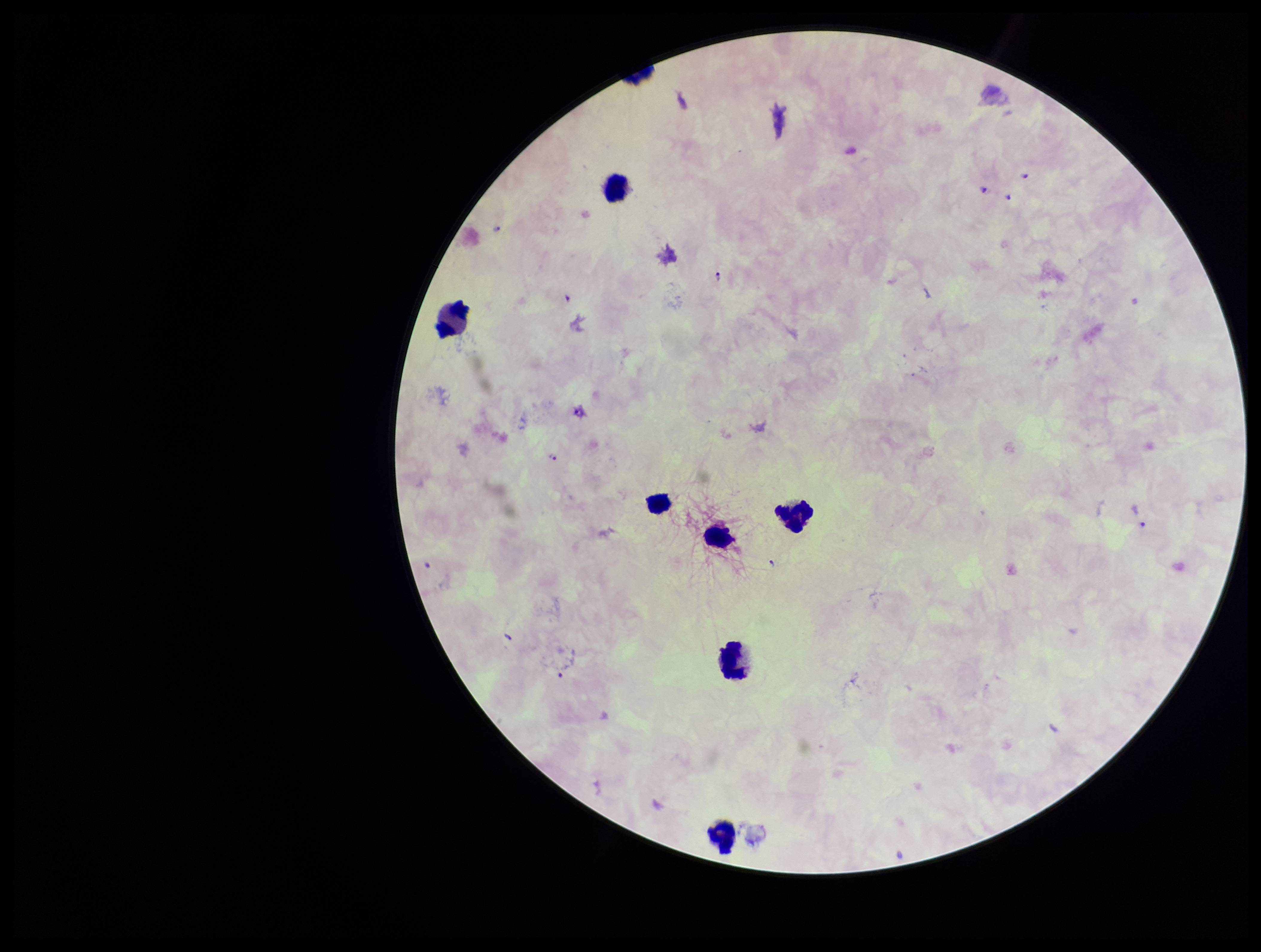
Summary:
  - Stain: Giemsa
  - Image size: 1261×952 pixels
  - Parasite count: 7
  - Species reported for this patient: Plasmodium falciparum
  - Preparation: thick
  - Patient malaria status: positive
  - Leukocyte count: 7
  - Capture: smartphone photograph through the microscope eyepiece
  - Plasmodium parasites: detected
  - Field of view: one from this slide